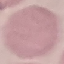

malaria status = uninfected
image type = automatically extracted cell patch, resized to 64 × 64 pixels
capture = smartphone camera at the microscope eyepiece
stain = Giemsa
preparation = thin blood smear